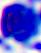 Photomicrograph. 400x magnification. A white blood cell is shown.